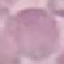

malaria status = uninfected
stain = Giemsa
capture = smartphone through the microscope eyepiece
preparation = thin blood smear
image type = automatically extracted cell patch, resized to 64 × 64 pixels